Name the blood parasite species.
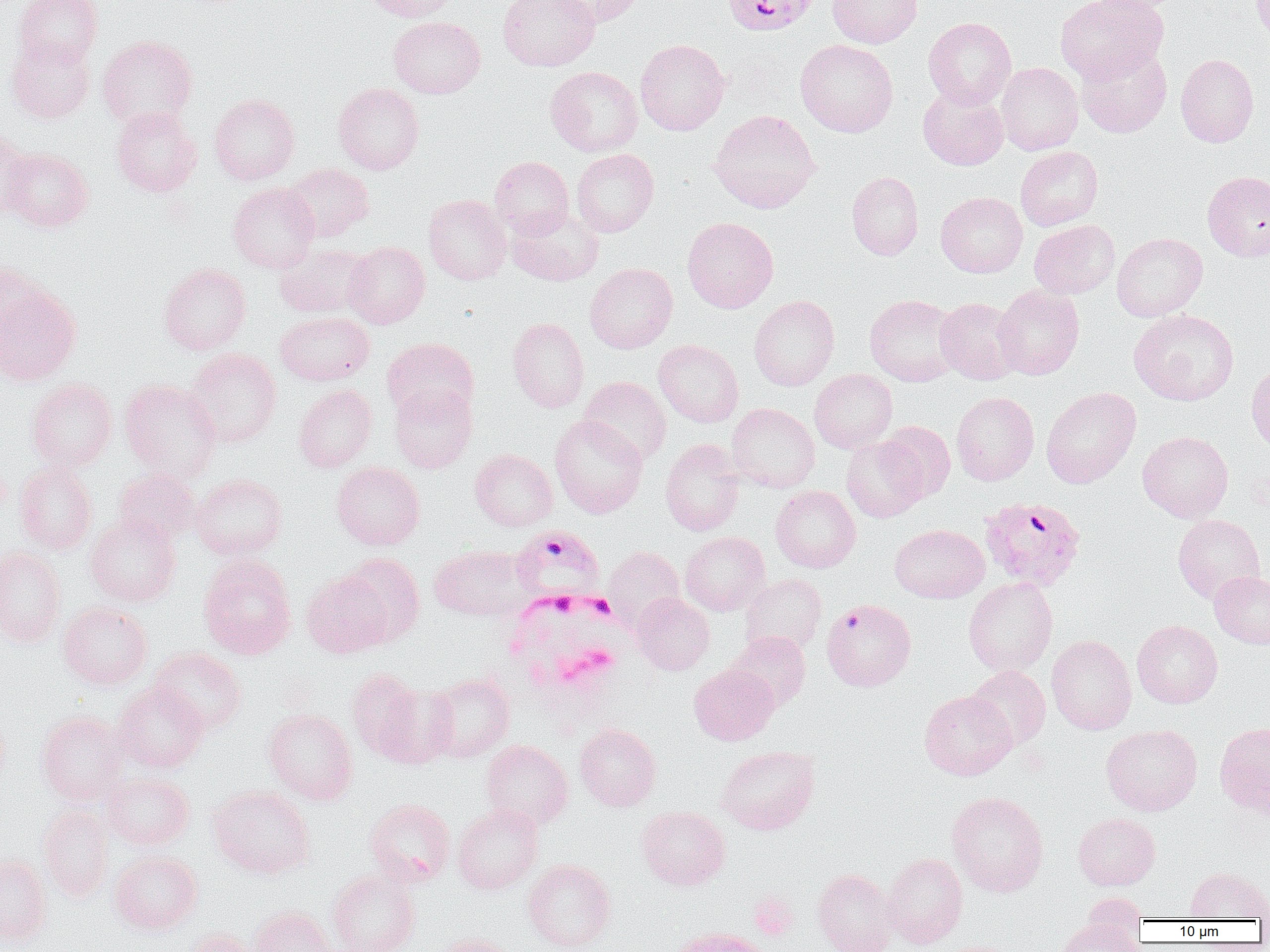

Plasmodium falciparum.

Summary:
  - Coordinate format: approximate bounding boxes as (x1, y1, x2, y2) in pixels
  - Uninfected red blood cell locations (subset): (14, 0, 103, 69), (361, 0, 459, 22), (498, 0, 600, 70), (548, 0, 646, 27), (827, 0, 923, 48), (1056, 0, 1167, 83), (1085, 0, 1180, 16), (1251, 0, 1270, 44), (389, 16, 486, 98), (923, 17, 1016, 108), (98, 35, 198, 129), (6, 36, 95, 123), (635, 39, 730, 135), (796, 39, 898, 137), (1076, 43, 1172, 137), (1176, 53, 1259, 147), (996, 62, 1083, 155), (546, 66, 643, 157), (333, 82, 424, 174), (918, 86, 1009, 170), (210, 94, 299, 184), (112, 105, 202, 197), (708, 109, 820, 213), (0, 127, 34, 221), (1015, 146, 1103, 231), (2, 147, 93, 231), (571, 148, 659, 237), (489, 156, 574, 239), (284, 163, 373, 242), (847, 171, 923, 260), (1202, 171, 1270, 261), (228, 182, 320, 273), (936, 192, 1027, 278), (424, 194, 511, 285), (507, 207, 603, 286), (682, 216, 778, 313), (1029, 220, 1119, 299), (1112, 232, 1207, 321), (344, 240, 430, 329), (275, 243, 373, 318), (0, 262, 43, 345), (159, 263, 250, 355), (584, 263, 678, 353), (0, 284, 81, 385), (994, 285, 1084, 380), (749, 295, 839, 391), (865, 295, 961, 386), (935, 297, 1023, 384), (1129, 309, 1239, 406), (275, 311, 374, 385), (508, 316, 589, 413), (382, 337, 479, 423), (653, 339, 744, 427), (184, 348, 281, 446), (1246, 361, 1270, 453), (809, 369, 897, 453), (578, 376, 671, 465), (27, 378, 117, 471), (120, 379, 222, 482), (294, 384, 377, 472), (389, 385, 477, 473), (1041, 386, 1141, 488), (951, 391, 1040, 485), (727, 403, 820, 493), (550, 415, 648, 518), (877, 421, 956, 502), (1137, 430, 1233, 522), (841, 436, 928, 522), (660, 439, 744, 535), (470, 449, 558, 531), (331, 461, 425, 550), (14, 464, 97, 555), (113, 469, 200, 546), (190, 474, 287, 560), (771, 486, 860, 572), (85, 514, 181, 607), (1172, 514, 1265, 603), (890, 524, 989, 603), (680, 531, 769, 615), (429, 545, 530, 621), (604, 546, 684, 630), (0, 547, 66, 647), (198, 553, 297, 660), (338, 553, 425, 647), (1209, 570, 1270, 648), (302, 571, 392, 658), (739, 573, 826, 656), (964, 577, 1057, 676), (632, 592, 715, 675), (58, 601, 153, 689), (1132, 620, 1223, 708), (727, 631, 811, 712), (1046, 634, 1137, 734), (150, 648, 247, 734), (689, 664, 779, 745), (966, 666, 1051, 749), (347, 668, 426, 759), (425, 672, 515, 762), (369, 678, 458, 768), (113, 681, 209, 772), (919, 690, 1017, 780), (264, 708, 357, 805), (37, 711, 128, 804), (574, 722, 661, 811), (1214, 722, 1270, 817), (1101, 724, 1202, 815), (480, 739, 573, 830), (716, 745, 819, 835), (102, 773, 194, 850), (208, 785, 314, 878), (946, 791, 1048, 897), (365, 798, 455, 886), (38, 804, 114, 902), (452, 804, 543, 895), (636, 805, 730, 891), (1073, 812, 1160, 890), (110, 850, 202, 934), (882, 852, 967, 948), (0, 853, 52, 947), (523, 859, 615, 951), (1185, 867, 1270, 920), (328, 868, 420, 952), (813, 868, 899, 952), (1081, 892, 1147, 945), (251, 906, 341, 952), (1056, 918, 1143, 952), (183, 928, 265, 952), (433, 934, 515, 952)
  - Plasmodium falciparum-infected red blood cell locations: (722, 0, 821, 36), (979, 496, 1085, 592), (511, 526, 606, 607), (822, 599, 916, 691)
  - White blood cell locations: (501, 589, 628, 703)
  - Preparation: thin blood film
  - Magnification: 1000x
  - Field of view: single
  - Image size: 1270×952 pixels
  - Modality: light microscopy